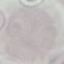
result: negative for malaria parasites
capture: smartphone through the microscope eyepiece
stain: Giemsa
image_type: cell patch, automatically extracted from a larger field of view and resized to 64 × 64 pixels
preparation: thin blood smear